State which parasite is depicted.
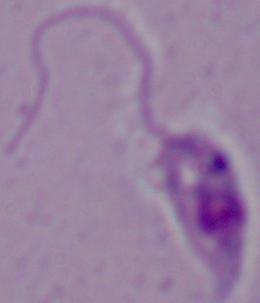

This is Leishmania.

modality = photomicrograph
magnification = 1000x